Assess this cell for malaria.
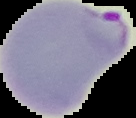
It is parasitized.

Image is 136×118 pixels. From a thin blood film. The area outside the segmented cell region is set to black.